Give the extent of all Plasmodium ovale-infected red blood cells.
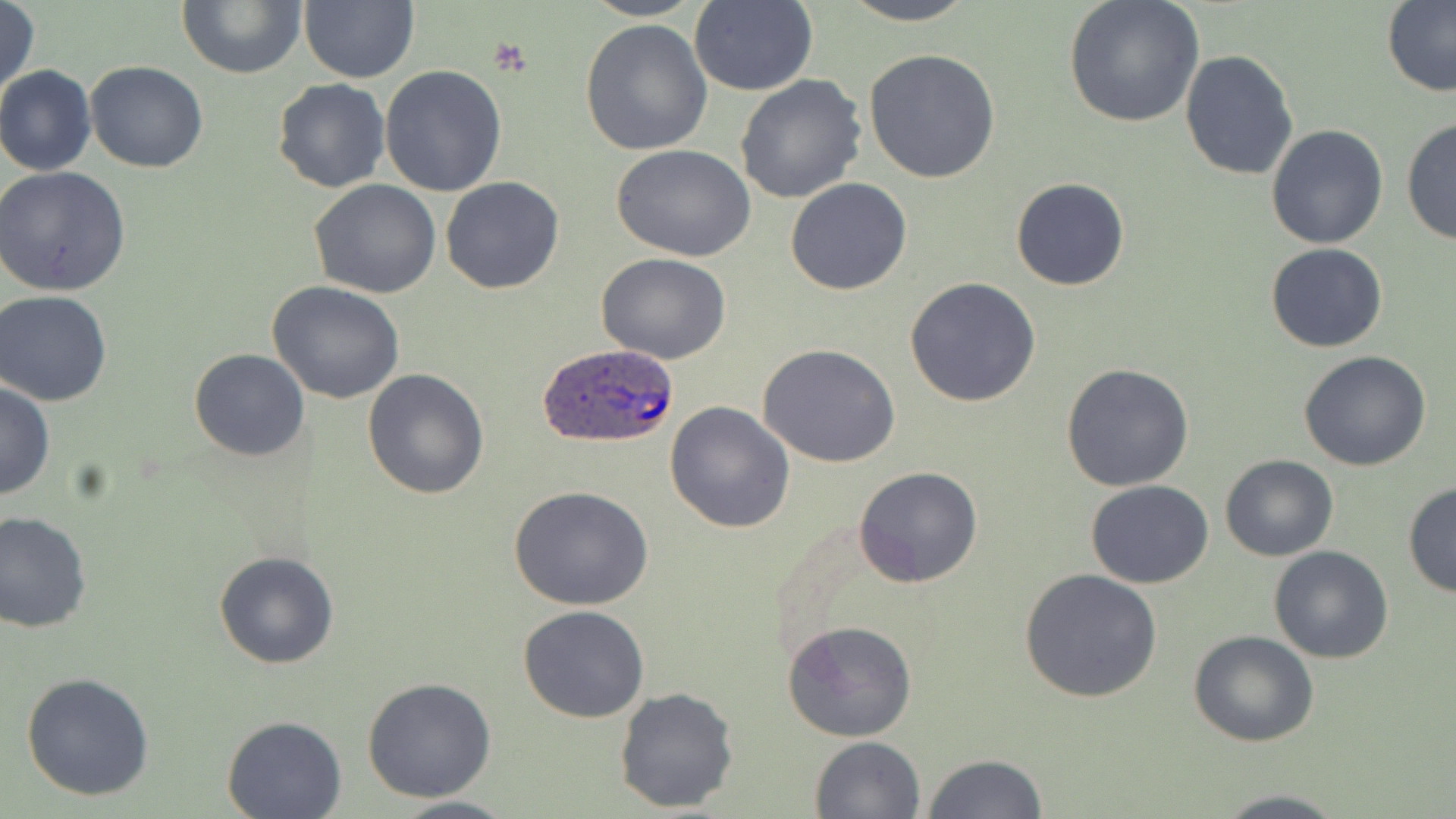

Approximate bounding boxes as named x1/y1/x2/y2 corners in pixels.
Plasmodium ovale-infected red blood cells: (x1=533, y1=341, x2=681, y2=451).

Platelet locations: (x1=488, y1=37, x2=536, y2=77). Uninfected red blood cell locations: (x1=299, y1=0, x2=418, y2=83), (x1=581, y1=0, x2=706, y2=21), (x1=838, y1=0, x2=977, y2=25), (x1=1063, y1=0, x2=1205, y2=127), (x1=1, y1=2, x2=41, y2=100), (x1=177, y1=2, x2=306, y2=78), (x1=687, y1=2, x2=818, y2=95), (x1=1381, y1=2, x2=1456, y2=97), (x1=580, y1=19, x2=714, y2=157), (x1=863, y1=48, x2=1001, y2=184), (x1=1178, y1=49, x2=1298, y2=182), (x1=85, y1=60, x2=208, y2=174), (x1=0, y1=65, x2=96, y2=178), (x1=379, y1=66, x2=507, y2=195), (x1=734, y1=74, x2=867, y2=204), (x1=272, y1=78, x2=390, y2=194), (x1=1401, y1=119, x2=1455, y2=244), (x1=1264, y1=124, x2=1390, y2=249), (x1=612, y1=146, x2=756, y2=261), (x1=0, y1=166, x2=131, y2=297), (x1=440, y1=176, x2=565, y2=294), (x1=1011, y1=177, x2=1129, y2=291), (x1=785, y1=178, x2=912, y2=295), (x1=309, y1=181, x2=441, y2=298), (x1=1265, y1=244, x2=1387, y2=352), (x1=596, y1=252, x2=732, y2=364), (x1=904, y1=278, x2=1041, y2=407), (x1=266, y1=281, x2=407, y2=404), (x1=1, y1=289, x2=117, y2=406), (x1=758, y1=343, x2=902, y2=467), (x1=189, y1=348, x2=309, y2=461), (x1=1298, y1=350, x2=1431, y2=471), (x1=1060, y1=363, x2=1195, y2=492), (x1=363, y1=368, x2=491, y2=500), (x1=0, y1=379, x2=54, y2=501), (x1=664, y1=400, x2=795, y2=534), (x1=1220, y1=455, x2=1339, y2=562), (x1=854, y1=466, x2=984, y2=588), (x1=1085, y1=479, x2=1214, y2=588), (x1=1402, y1=483, x2=1455, y2=597), (x1=510, y1=486, x2=655, y2=611), (x1=0, y1=508, x2=93, y2=633), (x1=1269, y1=545, x2=1396, y2=663), (x1=212, y1=550, x2=339, y2=669), (x1=1020, y1=566, x2=1165, y2=704), (x1=517, y1=605, x2=649, y2=721), (x1=783, y1=619, x2=917, y2=742), (x1=1189, y1=631, x2=1317, y2=747), (x1=21, y1=672, x2=154, y2=801), (x1=362, y1=677, x2=496, y2=803), (x1=614, y1=685, x2=740, y2=814), (x1=220, y1=715, x2=347, y2=819), (x1=809, y1=736, x2=927, y2=819), (x1=922, y1=753, x2=1049, y2=819), (x1=1208, y1=790, x2=1350, y2=819), (x1=381, y1=794, x2=520, y2=818). Slide-level diagnosis: Plasmodium ovale. Captured at 1000x magnification. May-Grünwald-Giemsa stain. Light microscopy. Thin blood smear. Image is 1456×819 pixels. One field of a larger specimen.